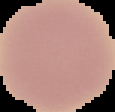
Summary:
  - Result: no Plasmodium parasites detected
  - Image type: cell region segmented out of the field of view; surrounding area masked to black
  - Preparation: thin blood film
  - Image size: 115×112 pixels